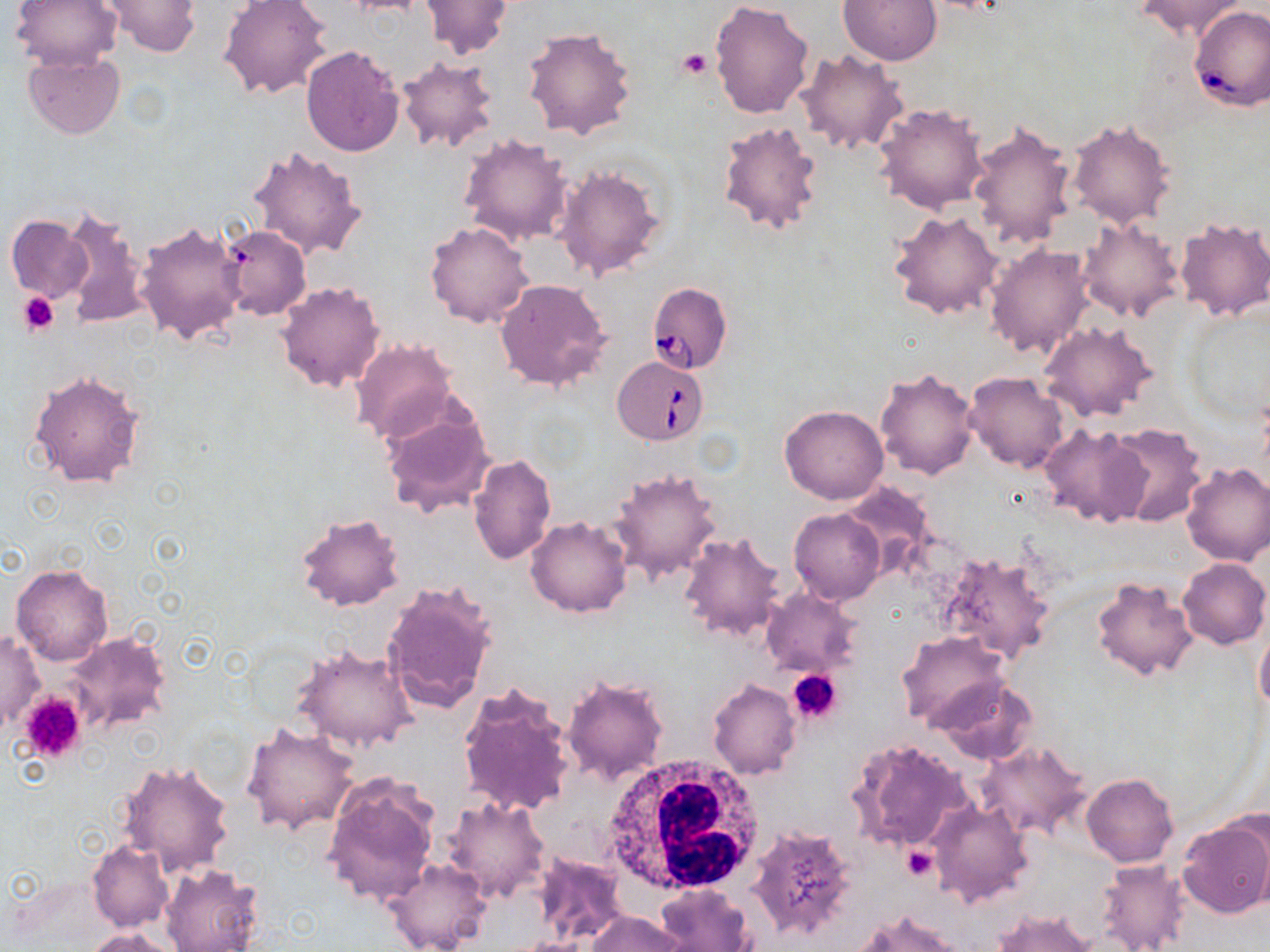 Approximate bounding boxes as (x1, y1, x2, y2) in pixels. Babesia divergens-infected red blood cell locations: (1188, 6, 1270, 111), (647, 282, 733, 375), (613, 355, 708, 444). Platelet locations: (677, 48, 712, 80), (18, 292, 58, 335), (787, 668, 843, 724), (20, 689, 89, 765), (900, 846, 938, 881). White blood cell locations: (601, 756, 766, 900). Uninfected red blood cell locations: (10, 0, 122, 71), (101, 0, 202, 56), (219, 0, 333, 102), (709, 0, 815, 119), (838, 0, 942, 65), (1136, 0, 1247, 39), (420, 1, 513, 60), (522, 27, 637, 142), (301, 45, 405, 156), (797, 49, 908, 155), (22, 51, 125, 139), (396, 55, 501, 156), (874, 103, 988, 214), (968, 118, 1079, 251), (1066, 118, 1175, 227), (716, 119, 825, 239), (457, 133, 575, 246), (247, 144, 367, 259), (552, 163, 667, 282), (59, 206, 152, 330), (889, 209, 1003, 320), (6, 214, 93, 303), (1175, 216, 1270, 322), (1077, 217, 1186, 323), (134, 221, 247, 345), (425, 221, 535, 329), (218, 225, 310, 320), (986, 243, 1094, 358), (494, 278, 612, 392), (275, 280, 384, 394), (1182, 304, 1270, 423), (1039, 320, 1159, 422), (352, 339, 459, 444), (875, 367, 980, 479), (27, 370, 146, 490), (964, 372, 1068, 472), (378, 400, 496, 518), (779, 405, 888, 505), (1104, 422, 1208, 526), (1039, 423, 1151, 527), (468, 453, 556, 565), (1180, 461, 1270, 565), (608, 467, 723, 583), (789, 508, 886, 605), (294, 512, 404, 613), (526, 517, 632, 616), (678, 531, 787, 644), (935, 551, 1056, 666), (1177, 557, 1269, 649), (10, 564, 111, 666), (1092, 576, 1198, 682), (382, 582, 497, 714), (759, 587, 864, 677), (1255, 625, 1270, 718), (1, 630, 44, 735), (62, 630, 170, 738), (896, 630, 1011, 730), (292, 641, 420, 754), (561, 674, 668, 786), (707, 678, 801, 780), (931, 678, 1038, 766), (457, 685, 576, 819), (243, 723, 360, 834), (848, 737, 975, 855), (977, 742, 1090, 840), (117, 759, 236, 876), (320, 774, 441, 907), (1082, 774, 1179, 867), (444, 797, 551, 902), (927, 799, 1033, 909), (1179, 814, 1270, 919), (747, 826, 859, 940), (87, 839, 174, 931), (531, 851, 628, 945), (384, 858, 490, 952), (1096, 859, 1191, 952), (159, 862, 265, 952), (655, 884, 754, 952), (992, 908, 1099, 952), (852, 910, 964, 952), (588, 911, 684, 952), (84, 927, 182, 952). Slide-level diagnosis: Babesia divergens. 1000x magnification. Light microscopy. Image is 1270×952 pixels. Thin blood film. Single field of view. May-Grünwald-Giemsa stain.